Give the extent of all uninfected red blood cells.
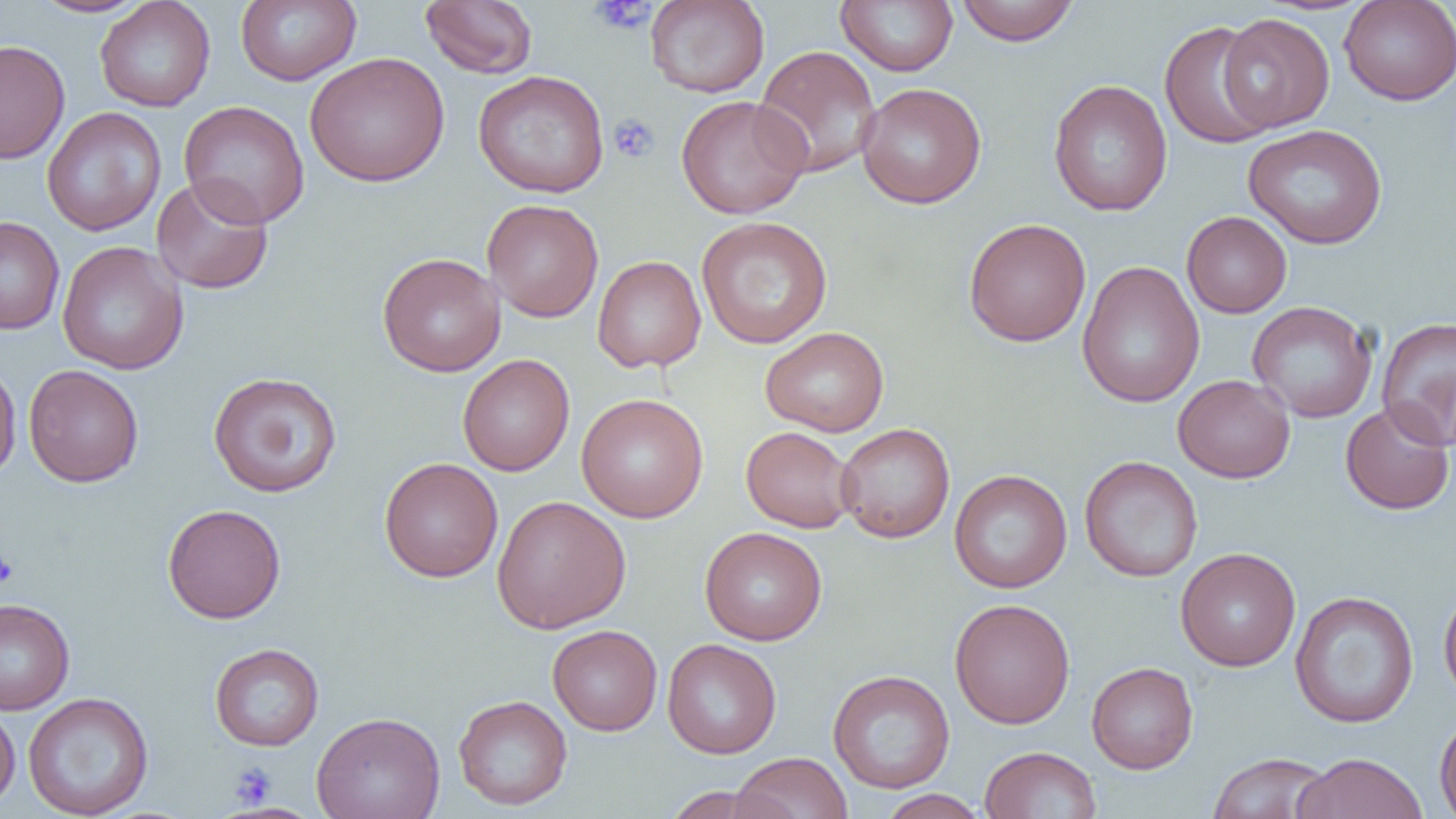
Approximate bounding boxes as (x1, y1, x2, y2) in pixels.
Uninfected red blood cells: (32, 0, 150, 17), (236, 0, 361, 85), (419, 0, 539, 79), (645, 0, 769, 97), (835, 0, 958, 76), (1339, 0, 1456, 105), (94, 1, 216, 112), (955, 1, 1080, 46), (1217, 13, 1335, 133), (1159, 20, 1276, 150), (0, 39, 70, 164), (753, 45, 882, 178), (304, 52, 449, 188), (473, 70, 610, 198), (1048, 80, 1173, 216), (856, 82, 987, 209), (676, 94, 812, 219), (179, 100, 310, 229), (41, 107, 167, 237), (1243, 124, 1388, 249), (151, 175, 274, 295), (481, 199, 604, 323), (1181, 211, 1292, 318), (0, 216, 65, 334), (697, 216, 833, 348), (963, 218, 1091, 347), (57, 241, 188, 375), (377, 252, 506, 377), (592, 255, 707, 372), (1077, 261, 1205, 409), (1247, 301, 1378, 423), (1376, 316, 1456, 451), (760, 326, 889, 437), (458, 354, 575, 476), (0, 358, 22, 481), (23, 365, 144, 487), (208, 371, 343, 497), (1173, 374, 1296, 483), (576, 393, 708, 523), (1339, 401, 1455, 515), (835, 423, 955, 543), (741, 426, 857, 533), (1079, 455, 1203, 583), (378, 457, 504, 582), (949, 469, 1072, 593), (491, 495, 631, 634), (162, 504, 286, 624), (699, 526, 827, 646), (1175, 547, 1301, 672), (1438, 582, 1456, 708), (1290, 590, 1419, 728), (0, 597, 75, 715), (949, 598, 1075, 729), (547, 624, 662, 735), (662, 639, 782, 759), (209, 642, 325, 751), (1086, 661, 1199, 773), (827, 669, 955, 793), (23, 692, 154, 818), (453, 694, 572, 810), (0, 704, 20, 812), (311, 711, 445, 819), (1434, 713, 1456, 819), (979, 746, 1102, 819), (730, 752, 853, 819), (1207, 752, 1333, 819), (1294, 752, 1428, 819), (661, 785, 782, 819), (877, 789, 989, 819).

{
  "slide_level_diagnosis": "no evidence of blood parasites",
  "platelet_locations": "approximate bounding boxes as (x1, y1, x2, y2) in pixels: (589, 0, 655, 35), (608, 113, 660, 163), (0, 551, 19, 589), (228, 761, 276, 808)",
  "modality": "optical microscopy",
  "image_size": "1456×819 pixels",
  "magnification": "1000x",
  "field_of_view": "one of a larger specimen",
  "preparation": "thin blood film"
}